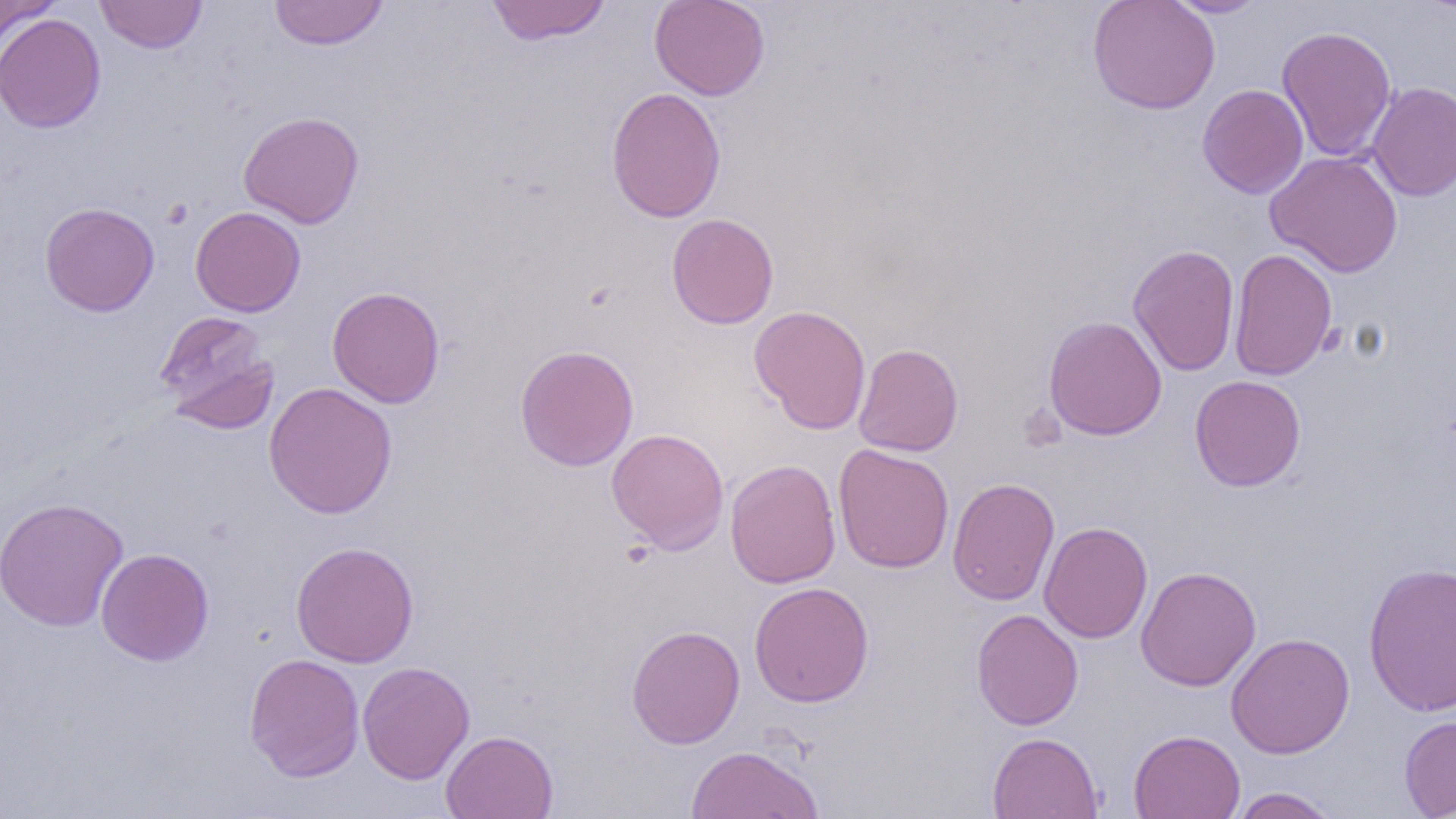

Approximate bounding boxes as [x1, y1, x2, y2] in pixels. Uninfected red blood cell locations: [94, 0, 208, 54], [485, 0, 612, 46], [649, 0, 770, 100], [1087, 0, 1220, 115], [1161, 0, 1269, 18], [0, 1, 58, 56], [268, 1, 389, 50], [0, 12, 106, 133], [1277, 25, 1397, 162], [1366, 81, 1456, 201], [1197, 84, 1309, 199], [606, 87, 726, 223], [238, 111, 365, 229], [1265, 151, 1403, 277], [39, 202, 160, 317], [190, 206, 306, 317], [666, 213, 779, 330], [1127, 244, 1240, 376], [1228, 247, 1338, 381], [327, 286, 445, 408], [749, 305, 871, 435], [153, 310, 279, 434], [1043, 315, 1167, 441], [853, 342, 964, 457], [514, 345, 639, 472], [1189, 375, 1306, 491], [263, 381, 398, 519], [606, 428, 730, 554], [832, 443, 955, 574], [725, 459, 841, 588], [947, 478, 1060, 605], [0, 496, 129, 632], [1039, 521, 1153, 643], [290, 541, 420, 668], [95, 547, 215, 666], [1362, 561, 1456, 717], [1136, 566, 1261, 691], [748, 582, 875, 707], [971, 609, 1084, 730], [627, 625, 745, 749], [1226, 632, 1355, 759], [243, 652, 365, 782], [357, 660, 475, 784], [1398, 714, 1456, 817], [441, 729, 559, 819], [1128, 729, 1246, 819], [987, 732, 1103, 819], [686, 744, 824, 818], [1231, 787, 1341, 818]. Platelet locations: [160, 199, 192, 229]. Slide-level diagnosis: negative for blood parasites. Thin blood film. 1000x magnification. Light microscopy. One field of a larger specimen. Image is 1456×819 pixels.